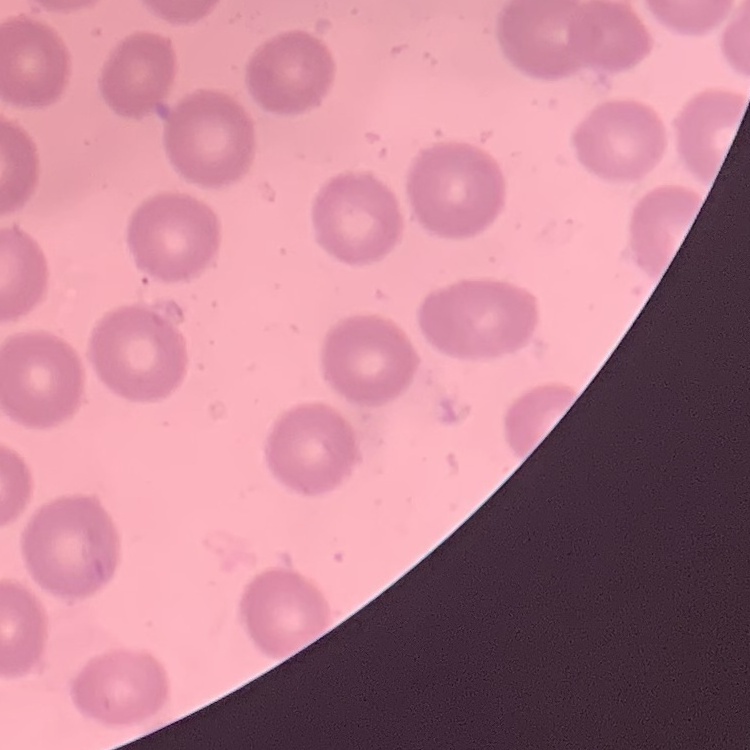

red blood cell morphology = no rouleaux formation
image type = square crop of a larger photomicrograph
stain = Field's or Giemsa
preparation = thin blood film